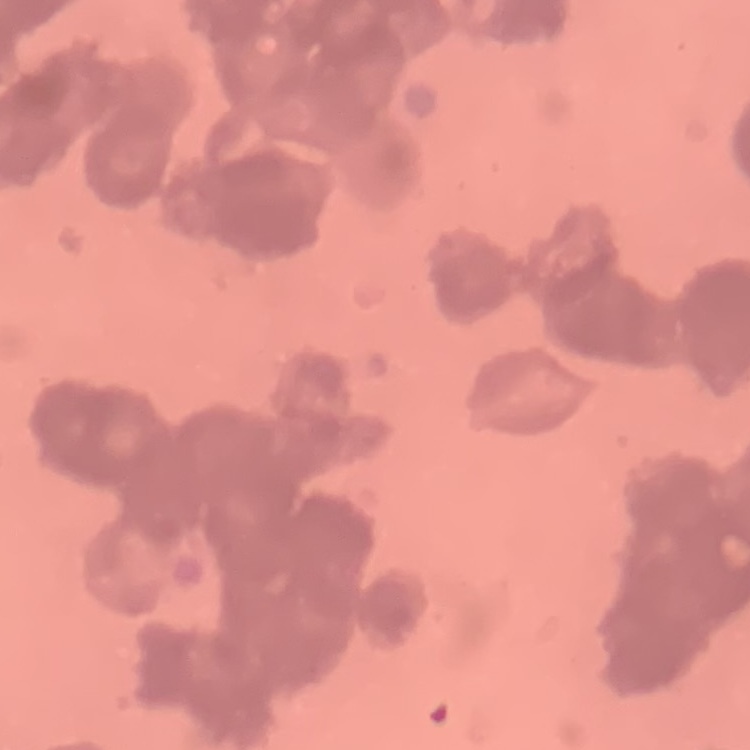

Summary:
  - Erythrocyte morphology: rouleaux formation
  - Preparation: thin blood film
  - Stain: Field's or Giemsa
  - Image type: one tile cut from a larger photomicrograph